Assess the morphology of the red blood cells.
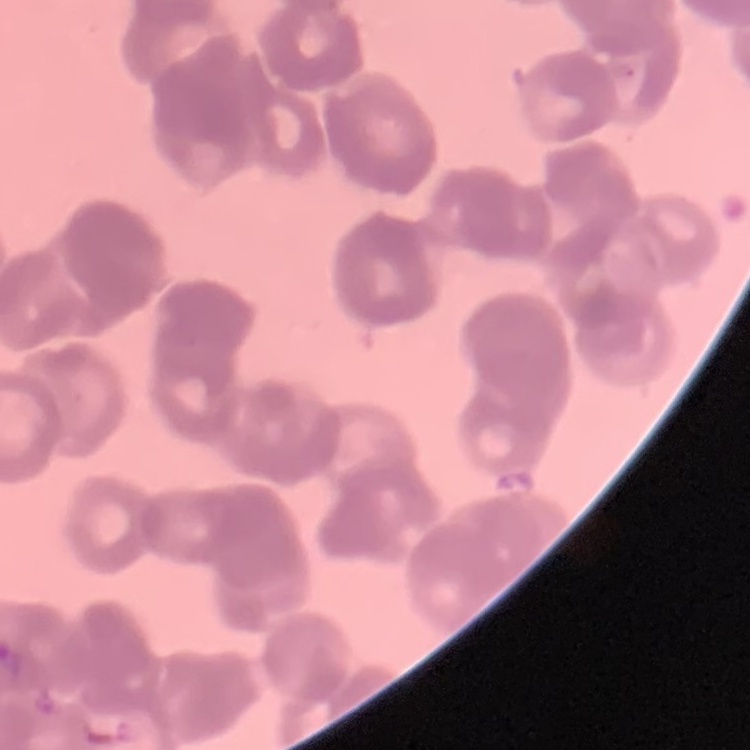

Rouleaux formation.

Field's or Giemsa stain. Thin blood smear. One tile cut from a larger photomicrograph.